Classify this cell by malaria status.
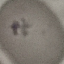

It is uninfected.

Acquired by smartphone through the microscope eyepiece. Cell patch, automatically extracted from a larger field of view and resized to 64 × 64 pixels. Giemsa stain. Thin smear of blood.